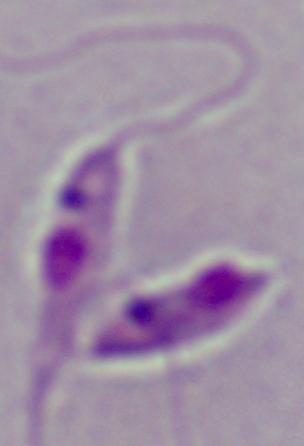

A Leishmania parasite is seen. Micrograph. Captured at 1000x magnification.